Assess the morphology of the red blood cells.
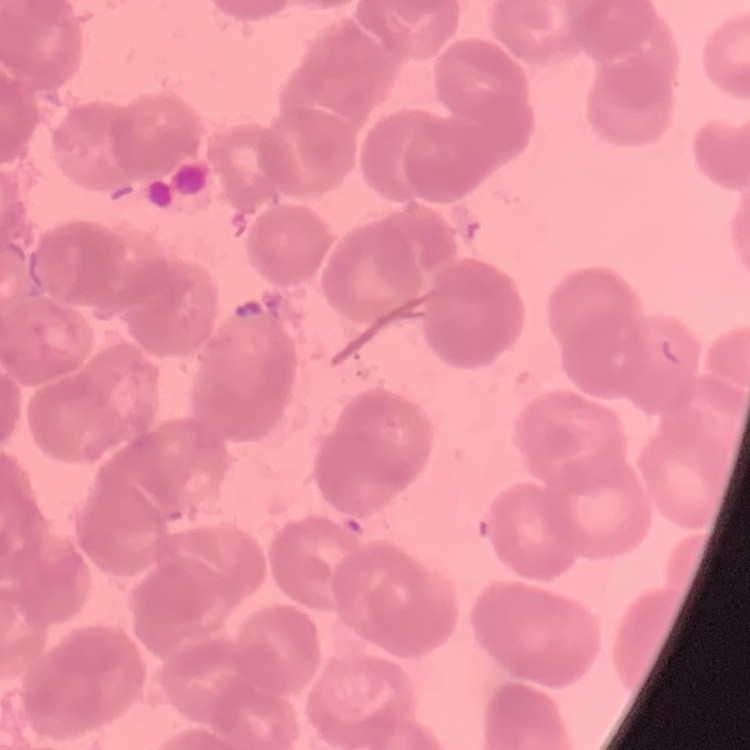
They show rouleaux formation.

Thin blood smear. One tile cut from a larger photomicrograph. Stained with either Field's or Giemsa.